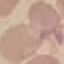

result: negative for malaria parasites
image_type: cell patch, automatically extracted from a larger field of view and resized to 64 × 64 pixels
stain: Giemsa
capture: smartphone camera at the microscope eyepiece
preparation: thin blood film